State which parasite is depicted.
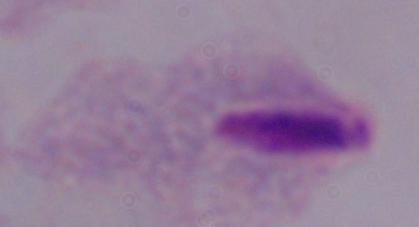

A trichomonad.

{
  "magnification": "1000x",
  "modality": "photomicrograph"
}